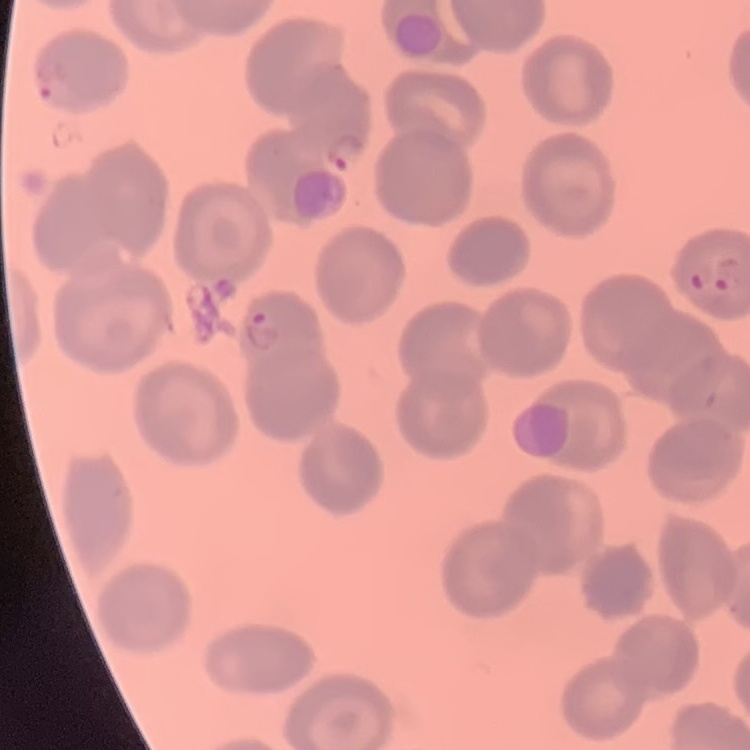
Summary:
  - Red blood cell morphology: no rouleaux formation
  - Preparation: thin blood smear
  - Image type: one tile cut from a larger photomicrograph
  - Stain: Field's or Giemsa